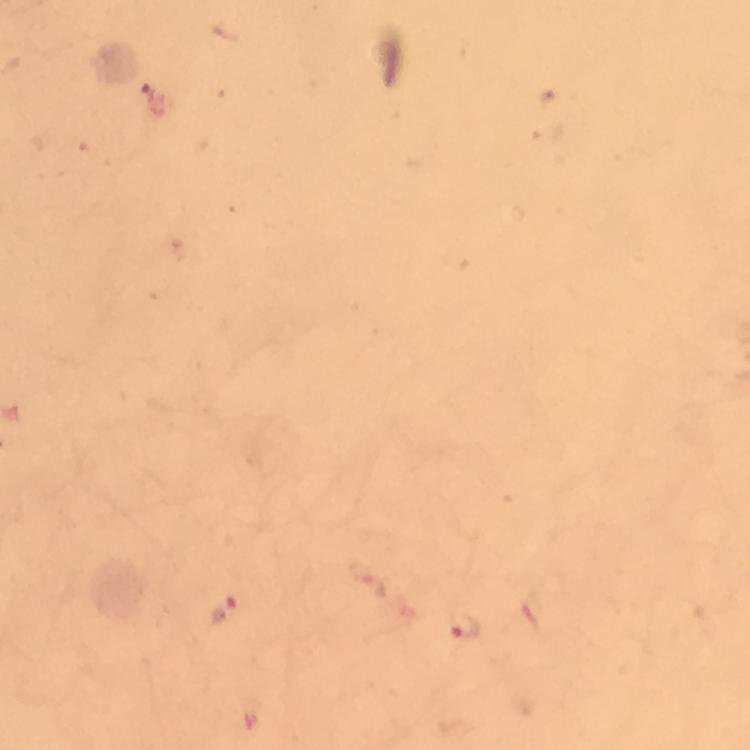
Approximate object centers, in pixels from the top-left corner.
Summary:
  - Plasmodium parasite locations: (x=463, y=630)
  - Capture: smartphone mounted on the microscope
  - Immersion oil: applied
  - Stain: Giemsa
  - Preparation: thick blood smear
  - Context: from a malaria diagnostic workup
  - Magnification: 100x
  - Cropped from: a single field of view
  - Image size: 750×750 pixels